Classify this cell by malaria status.
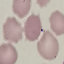
Uninfected.

preparation = thin blood film
stain = Giemsa
image type = cell patch, automatically extracted from a larger field of view and resized to 64 × 64 pixels
capture = smartphone through the microscope eyepiece